Report the malaria status of this cell.
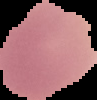
It is uninfected.

image size = 97×100 pixels
image type = segmented cell region with the area outside set to black
preparation = thin blood film